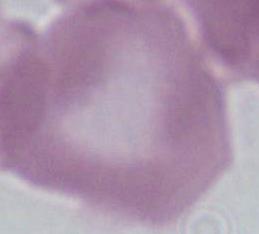

modality = photomicrograph
magnification = 1000x
identification = erythrocyte